Comment on the morphology of the erythrocytes.
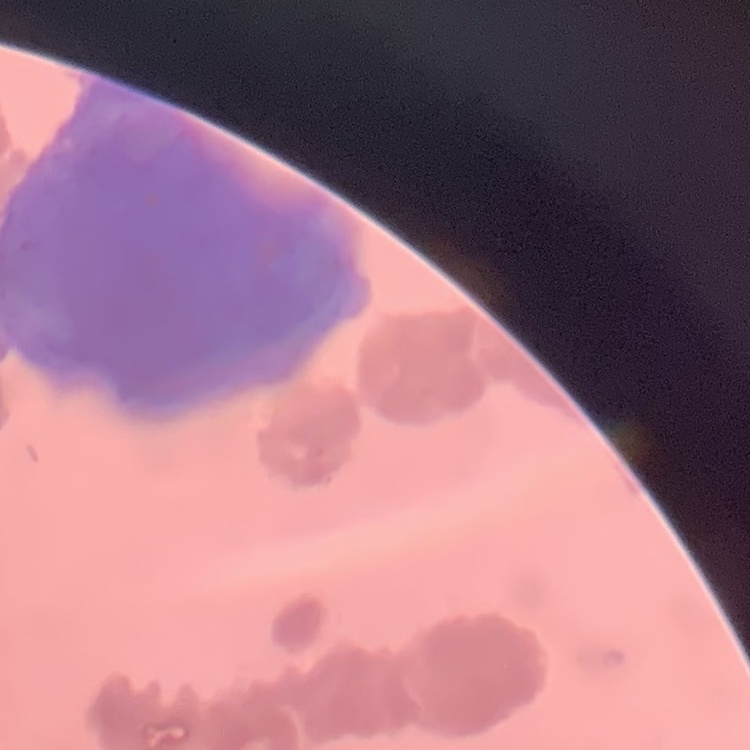

Rouleaux formation.

Thin blood smear. Field's or Giemsa stain. One tile cut from a larger photomicrograph.